Assess for parasitized red blood cells.
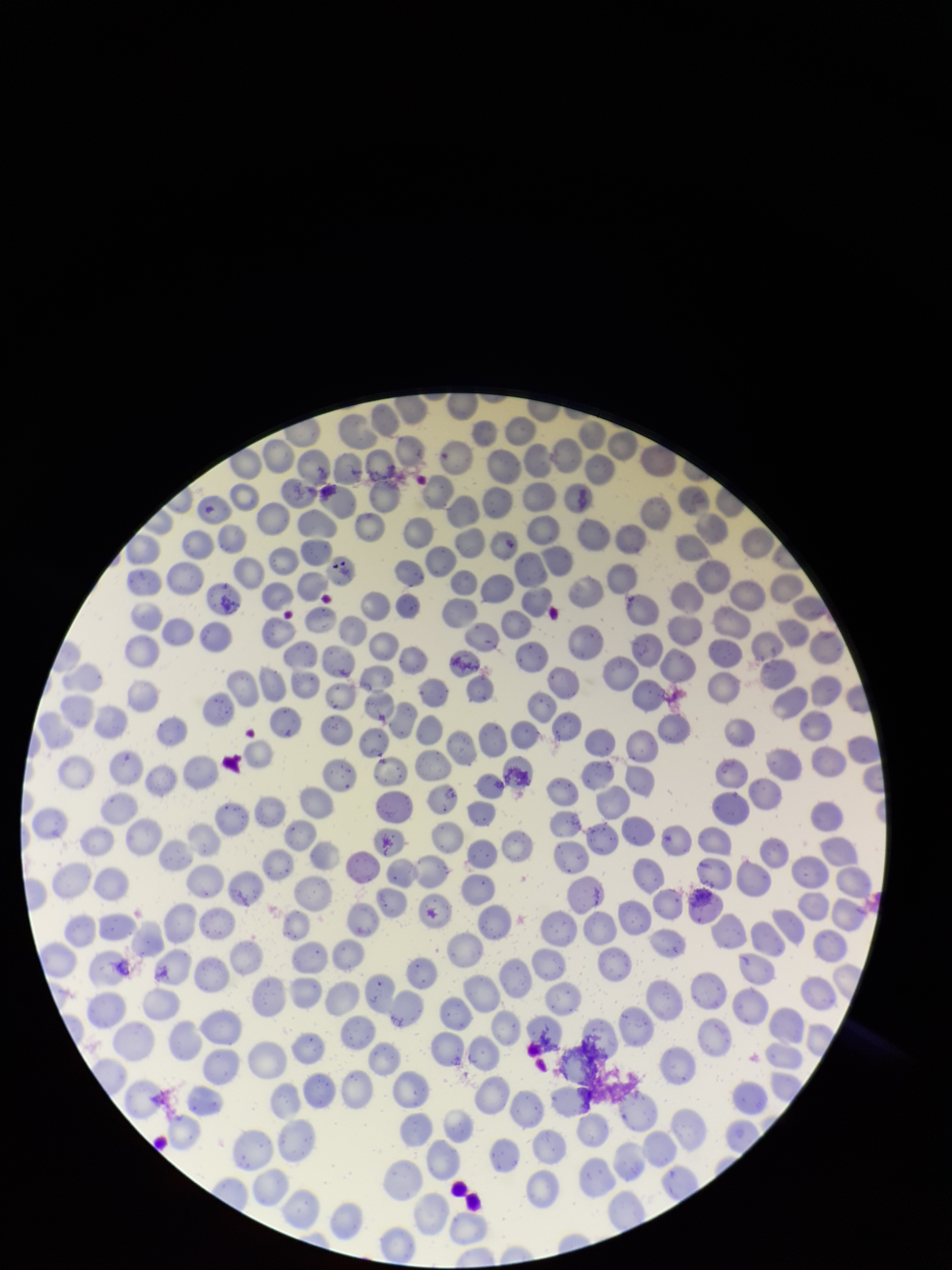

None seen.

Summary:
  - Image size: 952×1270 pixels
  - Preparation: thin
  - Parasitized red blood cell count: 0
  - Red blood cell count: 271
  - Patient malaria status: negative
  - Stain: Giemsa
  - Capture: smartphone photograph through the microscope eyepiece
  - Field of view: one from this slide